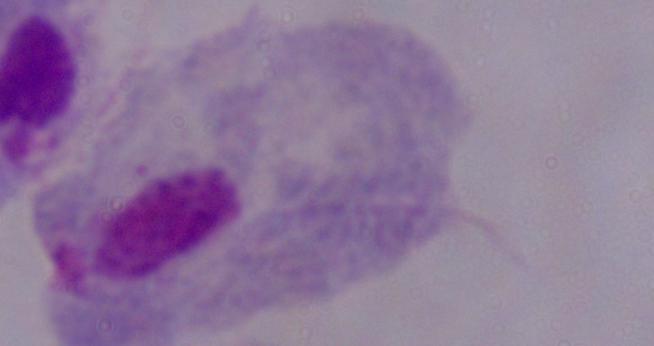
1000x magnification. A trichomonad is seen. Photomicrograph.